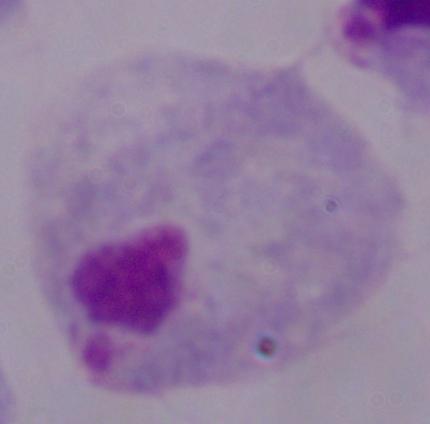
Captured at 1000x magnification. A trichomonad is shown. Micrograph.